State the preparation type.
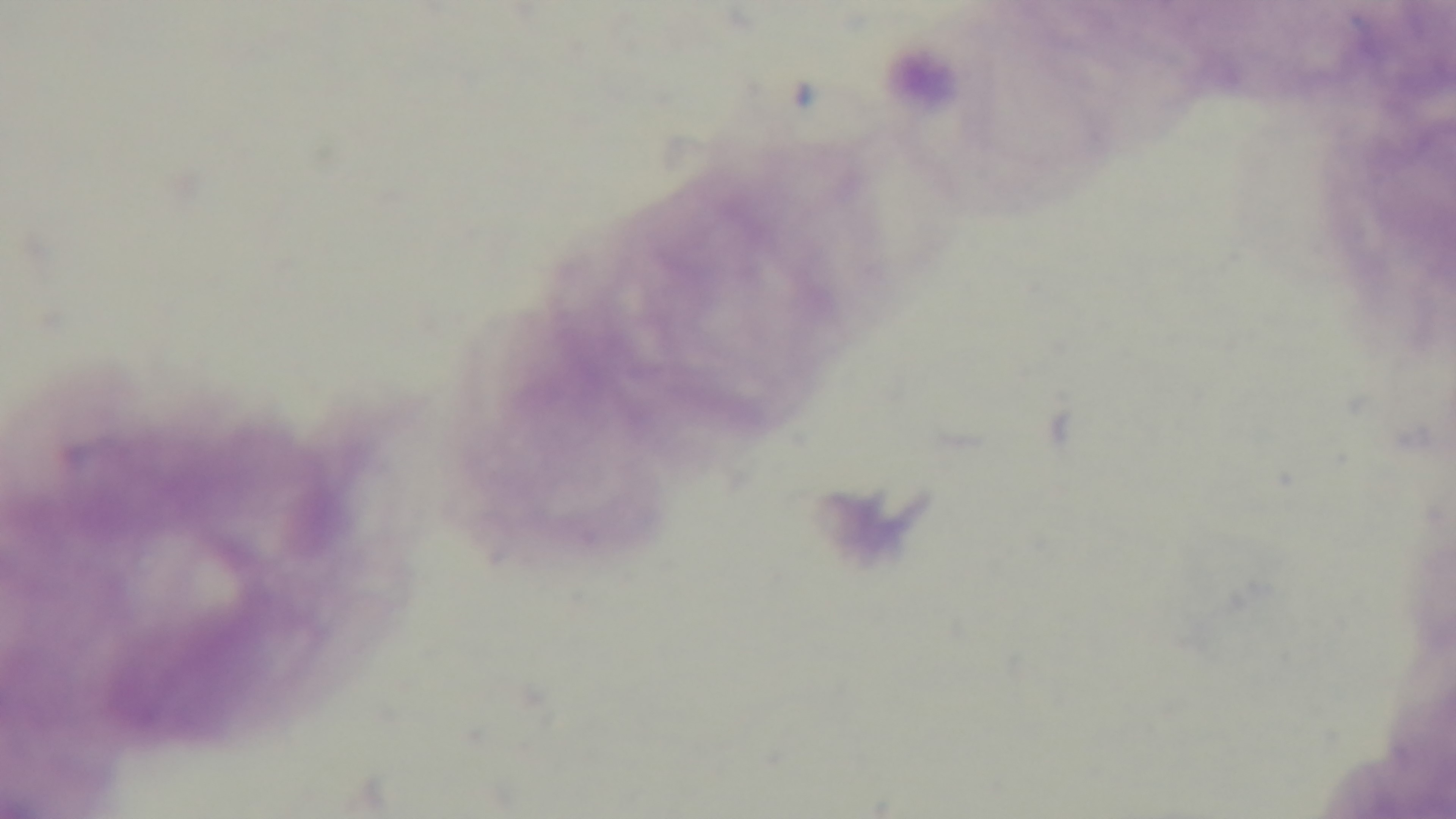
A thick smear.

Summary:
  - Stain: Giemsa
  - Capture: mounted 4K digital camera
  - Objective: 100x oil immersion
  - Malaria status: negative
  - Modality: light microscopy
  - Field of view: single